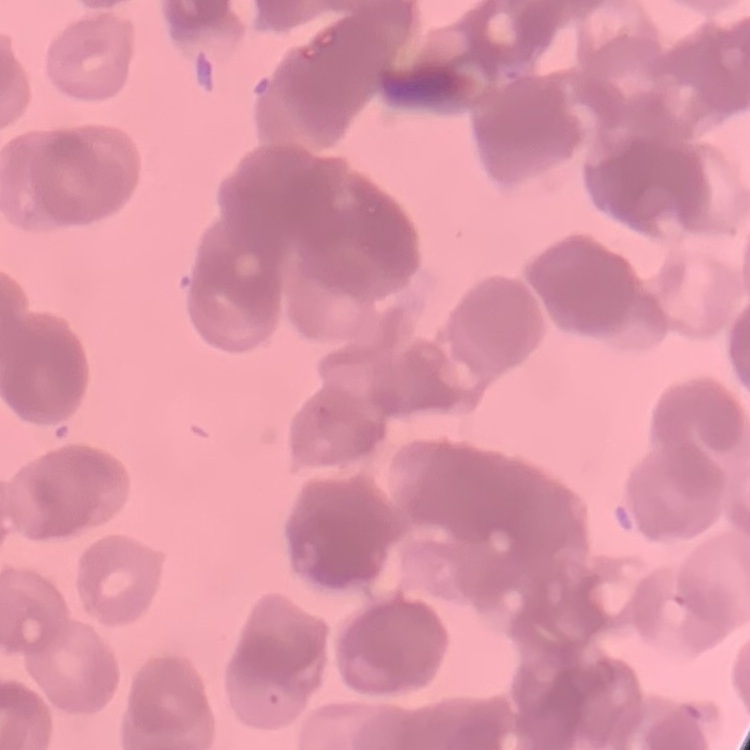 The erythrocytes show rouleaux formation. Field's or Giemsa stain. Square crop of a larger photomicrograph. Thin peripheral smear.